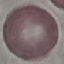

Malaria status: uninfected. Acquired by smartphone through the microscope eyepiece. Cell patch, automatically extracted from a larger field of view and resized to 64 × 64 pixels. Thin smear of blood. Giemsa stain.